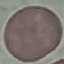

Summary:
  - Result: no malaria parasites seen
  - Image type: automatically extracted cell patch, resized to 64 × 64 pixels
  - Stain: Giemsa
  - Preparation: thin blood film
  - Capture: smartphone camera at the microscope eyepiece